Locate every uninfected red blood cell.
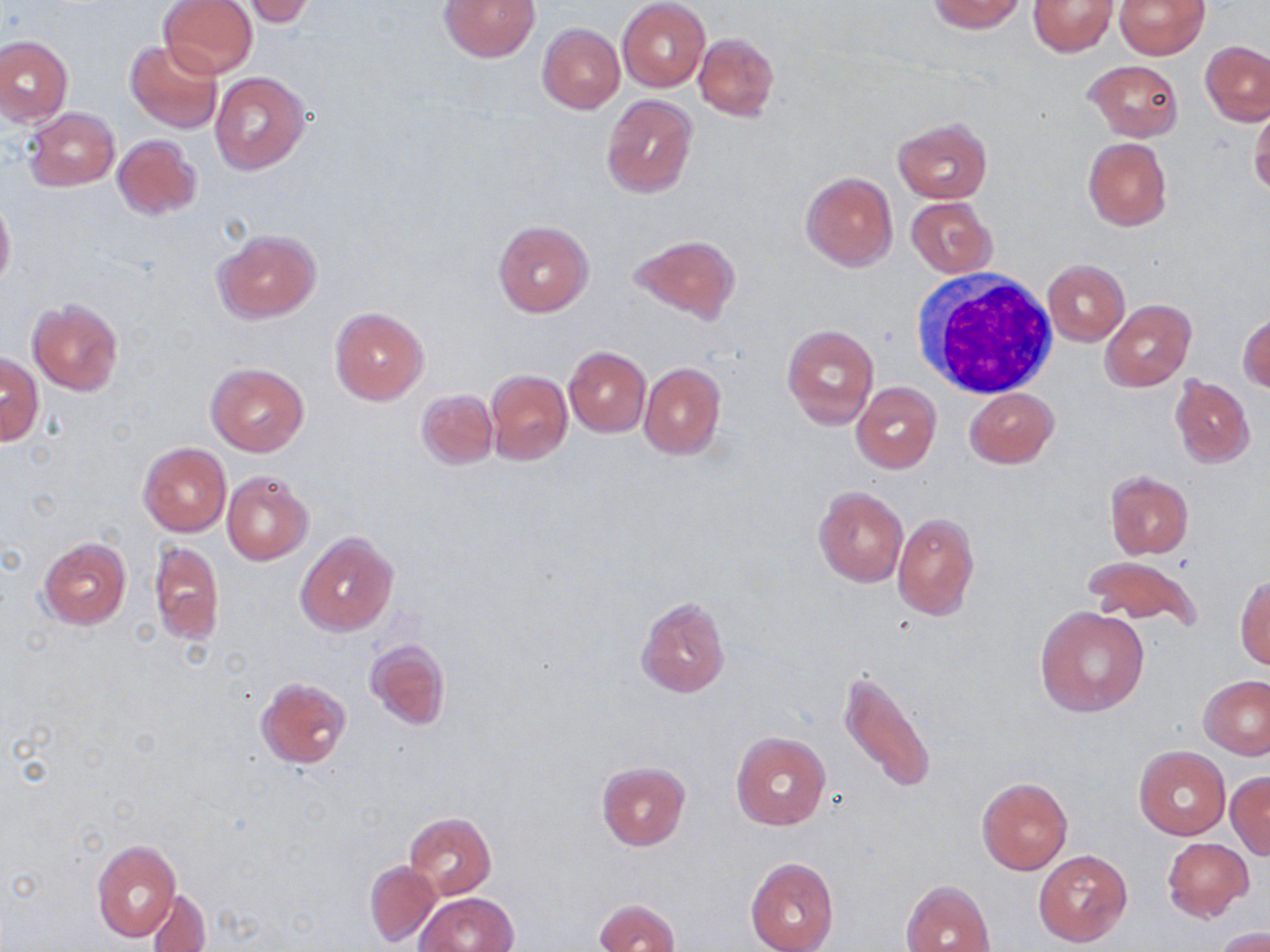

Approximate bounding boxes as [x1, y1, x2, y2] in pixels.
Uninfected red blood cells: [159, 0, 257, 78], [439, 0, 541, 62], [929, 0, 1026, 33], [1028, 0, 1117, 56], [1114, 0, 1210, 59], [240, 1, 316, 27], [617, 1, 709, 91], [537, 23, 624, 114], [694, 32, 778, 120], [0, 36, 72, 126], [125, 40, 224, 135], [1201, 41, 1270, 125], [1085, 60, 1183, 140], [210, 72, 309, 174], [601, 94, 698, 199], [1249, 104, 1270, 198], [24, 108, 120, 191], [894, 118, 993, 203], [112, 134, 201, 220], [1082, 138, 1173, 232], [801, 171, 898, 271], [0, 197, 14, 290], [907, 197, 996, 278], [493, 220, 593, 316], [213, 230, 319, 323], [631, 234, 740, 324], [1042, 259, 1129, 345], [1101, 299, 1196, 391], [29, 301, 122, 394], [329, 307, 429, 406], [1238, 314, 1270, 392], [782, 325, 879, 428], [563, 346, 650, 436], [1, 354, 42, 444], [207, 363, 309, 456], [639, 363, 726, 459], [486, 369, 572, 465], [1170, 375, 1256, 468], [850, 382, 941, 473], [965, 387, 1058, 469], [417, 389, 497, 469], [139, 443, 232, 537], [1104, 470, 1194, 559], [222, 472, 312, 564], [813, 486, 908, 587], [893, 512, 979, 620], [296, 532, 398, 636], [38, 536, 131, 629], [150, 540, 224, 645], [1083, 555, 1203, 630], [1235, 575, 1270, 669], [635, 595, 730, 698], [1036, 606, 1147, 717], [364, 639, 450, 730], [838, 669, 937, 795], [1199, 675, 1270, 760], [255, 676, 351, 769], [730, 732, 831, 830], [1133, 746, 1231, 840], [597, 762, 691, 850], [1227, 772, 1270, 859], [977, 777, 1073, 875], [405, 812, 495, 898], [1162, 838, 1253, 920], [90, 840, 180, 944], [1033, 849, 1132, 948], [745, 857, 838, 952], [364, 861, 442, 947], [901, 879, 995, 952], [146, 888, 210, 951], [418, 892, 519, 952], [594, 898, 680, 952], [1214, 927, 1270, 952].

Summary:
  - White blood cell locations: [909, 272, 1060, 399]
  - Slide-level diagnosis: no evidence of blood parasites
  - Field of view: single
  - Stain: May-Grünwald-Giemsa
  - Preparation: thin blood film
  - Image size: 1270×952 pixels
  - Modality: optical microscopy
  - Magnification: 1000x